State which parasite is depicted.
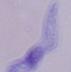

This is a trypanosome.

Captured at 1000x magnification. Photomicrograph.